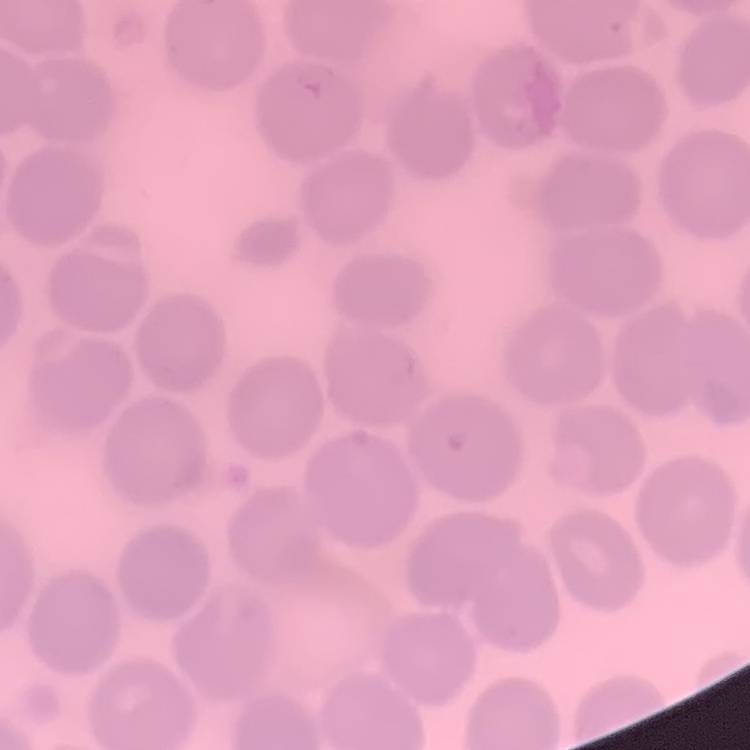

red blood cell morphology = no rouleaux formation
stain = Field's or Giemsa
image type = one tile cut from a larger photomicrograph
preparation = thin blood film